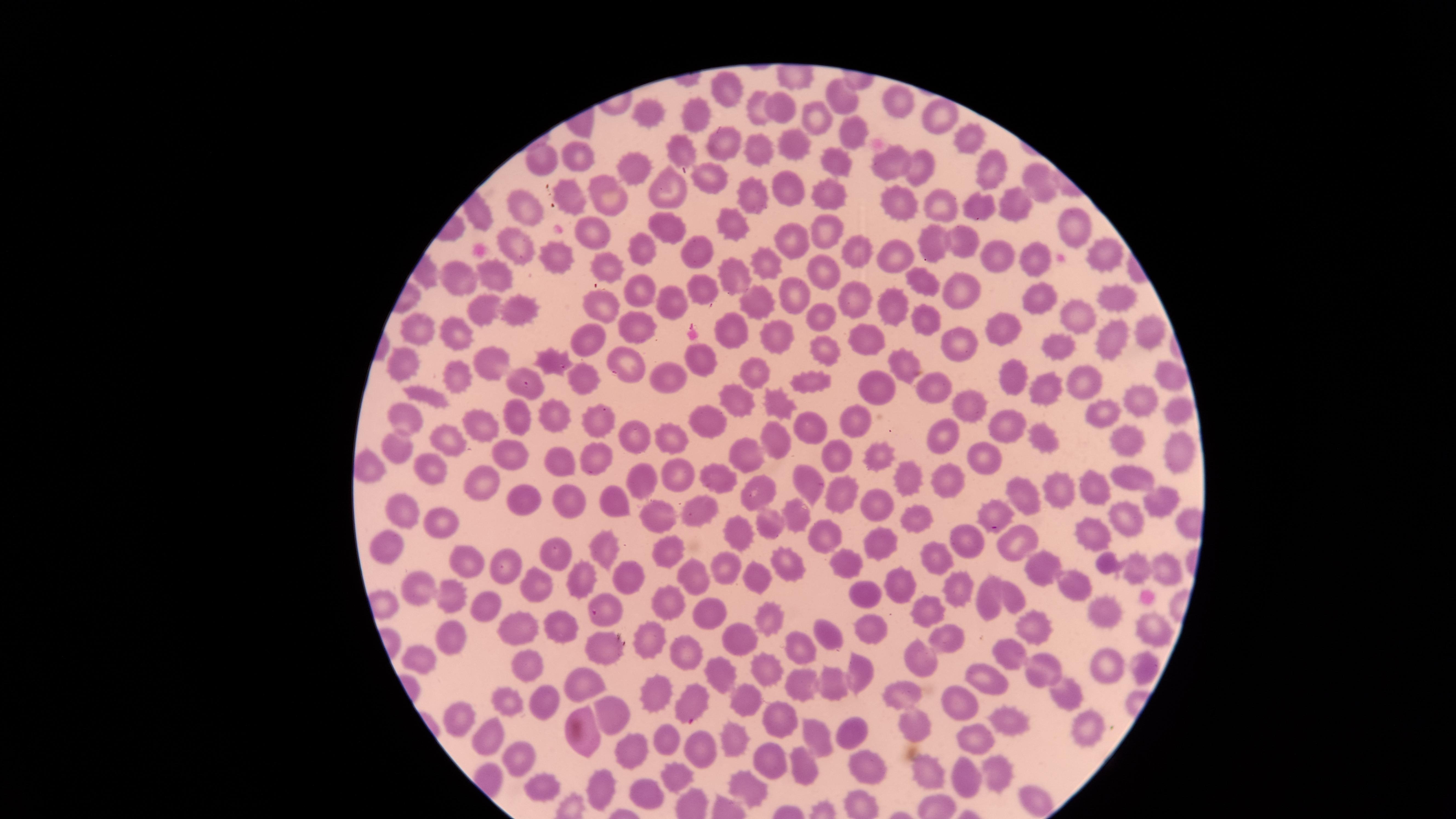

Approximate marker points as {x, y} in pixels. Uninfected red blood cells: {844, 92}, {727, 95}, {763, 103}, {898, 105}, {781, 106}, {649, 109}, {942, 112}, {699, 115}, {814, 115}, {852, 128}, {968, 136}, {794, 146}, {727, 147}, {761, 152}, {580, 155}, {681, 156}, {886, 160}, {834, 163}, {917, 164}, {992, 165}, {544, 167}, {637, 173}, {713, 179}, {1041, 179}, {569, 190}, {674, 190}, {791, 192}, {753, 197}, {826, 198}, {612, 199}, {901, 201}, {974, 203}, {945, 206}, {523, 207}, {1014, 207}, {728, 216}, {1070, 219}, {668, 228}, {827, 230}, {589, 234}, {793, 237}, {927, 242}, {968, 242}, {645, 247}, {521, 249}, {699, 249}, {852, 251}, {895, 254}, {1102, 254}, {993, 255}, {560, 260}, {1030, 260}, {611, 264}, {764, 265}, {823, 271}, {457, 275}, {735, 276}, {499, 277}, {922, 284}, {960, 289}, {1113, 289}, {704, 290}, {1036, 290}, {647, 293}, {792, 294}, {851, 297}, {666, 298}, {604, 305}, {757, 308}, {891, 308}, {521, 309}, {820, 314}, {488, 315}, {1073, 319}, {929, 321}, {1002, 324}, {641, 325}, {421, 329}, {731, 330}, {1149, 331}, {774, 334}, {461, 335}, {589, 340}, {867, 340}, {1061, 343}, {1113, 343}, {958, 345}, {824, 348}, {554, 356}, {695, 356}, {625, 357}, {401, 362}, {488, 362}, {905, 362}, {675, 370}, {1010, 372}, {1173, 372}, {585, 375}, {757, 375}, {1082, 378}, {456, 380}, {810, 380}, {933, 387}, {532, 388}, {875, 388}, {1047, 388}, {426, 393}, {739, 398}, {1137, 401}, {965, 402}, {776, 405}, {1103, 411}, {1175, 412}, {554, 415}, {595, 417}, {402, 419}, {519, 419}, {856, 420}, {712, 424}, {1008, 425}, {482, 426}, {807, 427}, {640, 438}, {679, 438}, {776, 438}, {1044, 438}, {1122, 438}, {447, 440}, {943, 443}, {397, 450}, {502, 450}, {835, 451}, {1178, 452}, {879, 454}, {981, 454}, {596, 456}, {752, 456}, {559, 457}, {429, 466}, {372, 470}, {676, 474}, {726, 475}, {907, 477}, {1128, 477}, {483, 478}, {650, 480}, {817, 481}, {1094, 481}, {762, 486}, {943, 486}, {1061, 491}, {1024, 493}, {844, 494}, {530, 495}, {621, 495}, {1159, 500}, {878, 502}, {569, 504}, {698, 509}, {650, 510}, {413, 511}, {911, 514}, {994, 514}, {796, 515}, {770, 519}, {1128, 521}, {445, 522}, {740, 532}, {824, 533}, {1095, 535}, {1011, 540}, {971, 541}, {879, 543}, {605, 546}, {386, 547}, {668, 551}, {558, 552}, {939, 555}, {783, 558}, {467, 563}, {848, 563}, {505, 564}, {1041, 564}, {1168, 565}, {726, 570}, {1134, 572}, {698, 575}, {585, 577}, {626, 577}, {759, 578}, {898, 582}, {1072, 583}, {533, 585}, {954, 585}, {420, 590}, {860, 592}, {445, 594}, {1010, 594}, {672, 602}, {990, 602}, {490, 606}, {930, 608}, {710, 611}, {1107, 611}, {607, 613}, {769, 620}, {1029, 623}, {559, 625}, {522, 626}, {869, 627}, {1149, 628}, {948, 631}, {825, 633}, {737, 635}, {453, 638}, {652, 639}, {794, 645}, {599, 647}, {677, 649}, {1007, 657}, {423, 659}, {917, 661}, {526, 663}, {1106, 663}, {1140, 665}, {764, 669}, {1043, 669}, {720, 670}, {859, 670}, {803, 681}, {994, 681}, {579, 683}, {833, 684}, {659, 689}, {1061, 690}, {903, 691}, {744, 694}, {510, 698}, {552, 702}, {692, 704}, {961, 704}, {774, 717}, {1007, 719}, {457, 720}, {617, 720}, {912, 725}, {1084, 729}, {850, 734}, {583, 736}, {671, 736}, {813, 736}, {733, 739}, {977, 741}, {490, 742}, {627, 745}, {703, 748}, {516, 754}, {764, 757}, {807, 766}, {864, 766}, {681, 772}, {996, 772}, {927, 774}, {964, 777}, {601, 785}, {746, 786}, {540, 787}, {637, 788}, {1032, 799}. Image is 1456×819 pixels. Presence: no malaria parasites detected. Thin blood film. Smartphone photograph through the microscope eyepiece. The visible region is circular. Single field of view. Giemsa-stained preparation.